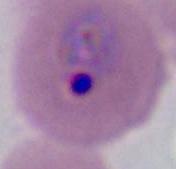

identification = Plasmodium
modality = photomicrograph
magnification = 400x or 1000x